Report the malaria status of this cell.
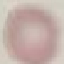

It is uninfected.

Cell patch, automatically extracted from a larger field of view and resized to 64 × 64 pixels. Thin blood film. Giemsa-stained preparation. Acquired by smartphone through the microscope eyepiece.